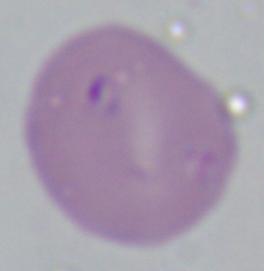
Summary:
  - Identification: Babesia
  - Modality: photomicrograph
  - Magnification: 1000x